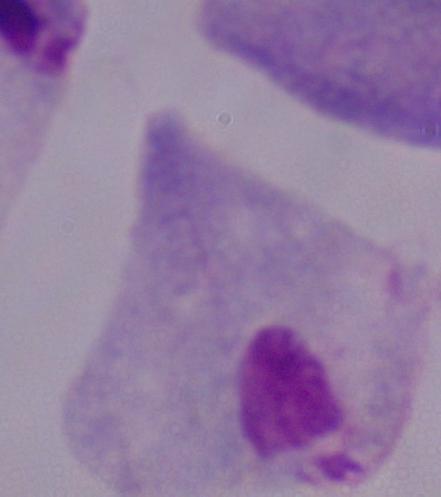

Summary:
  - Identification: trichomonad
  - Magnification: 1000x
  - Modality: photomicrograph